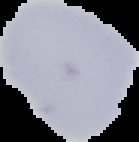
Summary:
  - Result: no malaria parasites seen
  - Image size: 139×142 pixels
  - Image type: segmented cell region on a black background
  - Preparation: thin blood film